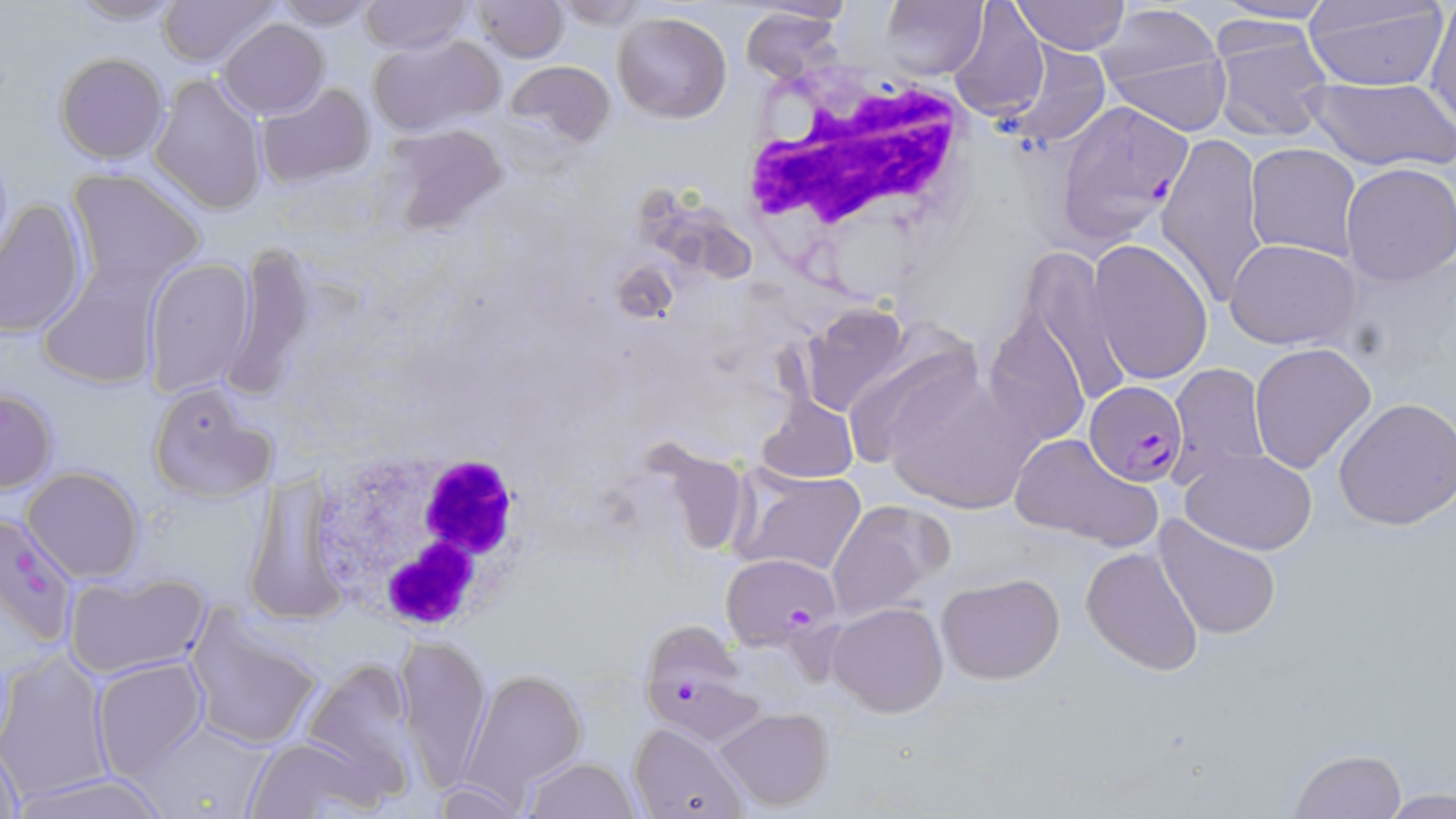

Plasmodium falciparum-infected red blood cell locations = approximate bounding boxes as [x1, y1, x2, y2] in pixels: [1053, 97, 1193, 246], [1085, 382, 1186, 484], [1, 511, 80, 649], [719, 551, 842, 650], [637, 618, 750, 728]
slide-level diagnosis = Plasmodium falciparum
magnification = 1000x
field of view = one of a larger specimen
stain = May-Grünwald-Giemsa
preparation = thin blood smear
image size = 1456×819 pixels
uninfected red blood cell locations = approximate bounding boxes as [x1, y1, x2, y2] in pixels: [62, 0, 186, 25], [156, 0, 279, 68], [471, 0, 568, 64], [880, 0, 986, 80], [1013, 0, 1130, 55], [1013, 0, 1212, 70], [1209, 0, 1337, 26], [272, 1, 379, 28], [359, 1, 471, 53], [553, 1, 652, 26], [1302, 1, 1449, 92], [948, 2, 1050, 123], [1427, 2, 1456, 128], [740, 6, 844, 85], [1098, 10, 1232, 133], [611, 11, 732, 123], [1211, 17, 1334, 142], [217, 18, 329, 117], [367, 36, 507, 136], [998, 42, 1110, 148], [55, 53, 167, 164], [502, 57, 618, 154], [149, 74, 268, 217], [1305, 77, 1456, 171], [256, 83, 376, 186], [380, 121, 511, 235], [1156, 131, 1269, 307], [1246, 143, 1362, 261], [1340, 164, 1456, 284], [66, 168, 205, 293], [0, 198, 88, 338], [1089, 238, 1214, 384], [1226, 240, 1360, 349], [221, 244, 320, 396], [1026, 247, 1130, 412], [144, 257, 255, 397], [36, 265, 161, 391], [801, 305, 913, 414], [983, 312, 1091, 450], [840, 335, 987, 474], [1248, 342, 1376, 473], [1167, 363, 1270, 490], [880, 364, 1042, 515], [147, 381, 274, 503], [0, 388, 56, 493], [756, 393, 858, 485], [1333, 395, 1456, 530], [1009, 432, 1163, 551], [1180, 449, 1317, 553], [22, 465, 144, 582], [734, 466, 864, 577], [827, 499, 951, 621], [1154, 516, 1279, 639], [1081, 546, 1202, 675], [63, 570, 209, 677], [937, 572, 1065, 683], [827, 601, 948, 716], [183, 606, 324, 753], [395, 634, 492, 790], [0, 652, 113, 802], [297, 657, 423, 797], [92, 658, 208, 782], [460, 667, 588, 800], [716, 707, 835, 811], [144, 719, 274, 814], [628, 722, 750, 819], [244, 734, 378, 817], [1, 739, 25, 818], [1288, 749, 1407, 819], [522, 756, 641, 819], [13, 771, 174, 819]
modality = light microscopy
white blood cell locations = approximate bounding boxes as [x1, y1, x2, y2] in pixels: [739, 63, 978, 268], [311, 441, 534, 634]